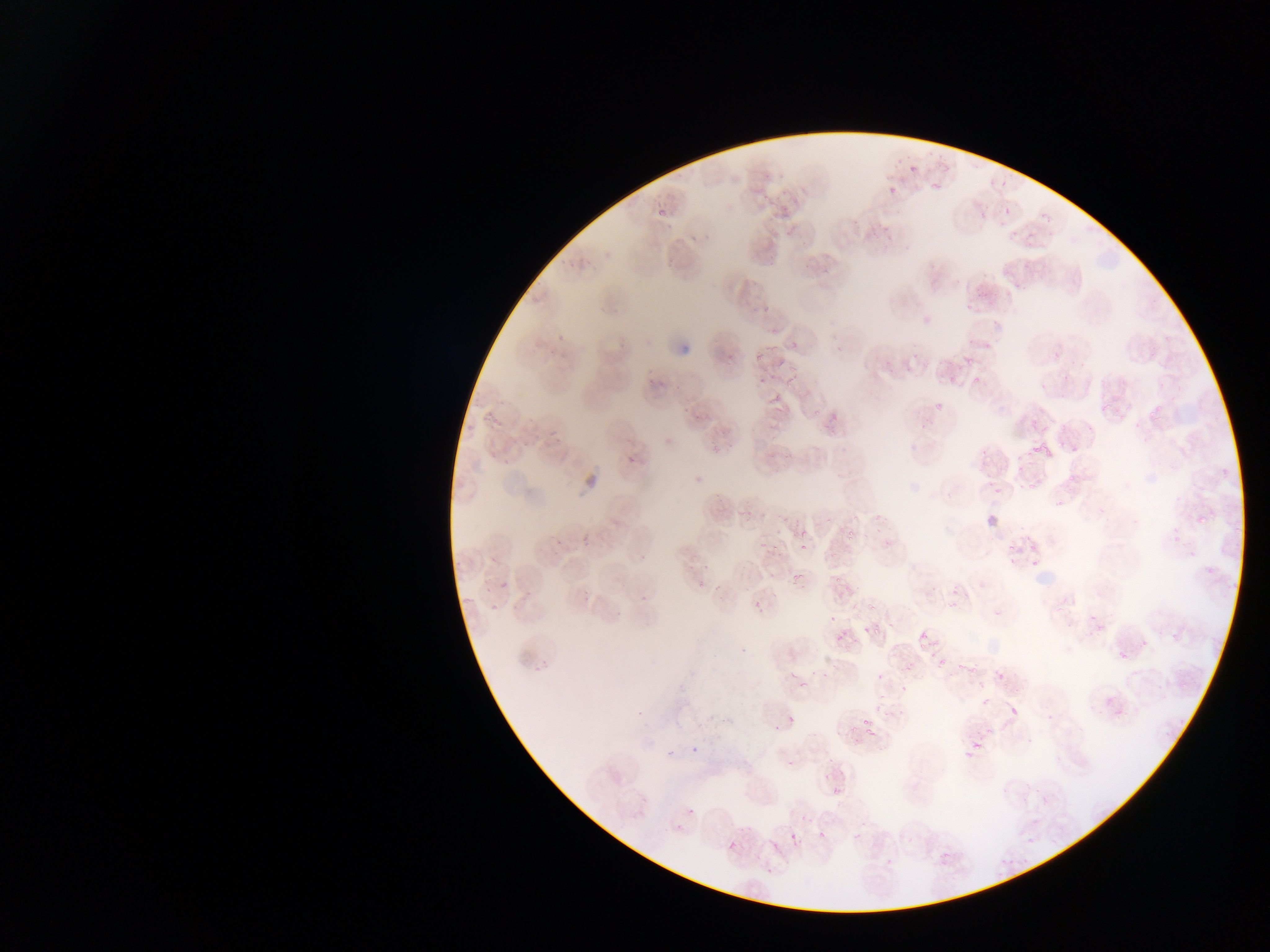
Plasmodium parasite locations = approximate bounding boxes as {left, top, right, bottom} in pixels: {908, 163, 917, 176}, {982, 180, 998, 194}, {884, 186, 894, 196}, {1003, 199, 1013, 214}, {977, 214, 992, 229}, {830, 220, 847, 234}, {1010, 224, 1025, 246}, {921, 314, 935, 329}, {757, 369, 772, 384}, {933, 398, 946, 415}, {1029, 435, 1056, 458}, {620, 455, 637, 466}, {795, 536, 809, 550}, {996, 537, 1026, 570}, {792, 572, 804, 584}, {632, 591, 648, 606}, {861, 621, 874, 636}, {917, 631, 931, 640}, {1116, 641, 1133, 669}, {1102, 700, 1110, 709}, {1005, 702, 1024, 723}, {783, 703, 801, 731}, {857, 715, 875, 733}, {661, 741, 672, 758}, {970, 741, 993, 756}, {691, 743, 702, 757}, {956, 750, 972, 766}, {825, 784, 838, 795}, {685, 806, 702, 814}, {672, 817, 684, 834}, {813, 827, 826, 841}, {786, 828, 799, 845}, {767, 838, 778, 854}, {726, 840, 740, 855}, {765, 865, 774, 876}
country = Ghana
preparation = thin blood film
image size = 1270×952 pixels
capture = mobile-phone photograph through a microscope
field of view = single